Assess this cell for malaria.
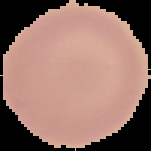
It is uninfected.

Image is 151×151 pixels. From a thin blood film. The area outside the segmented cell region is set to black.